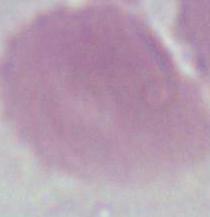
magnification = 1000x
modality = micrograph
identification = red blood cell